Assess this cell for malaria.
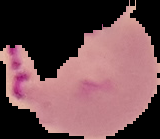

Parasitized.

Summary:
  - Preparation: thin blood film
  - Image type: cell region segmented out of the field of view; surrounding area masked to black
  - Image size: 160×139 pixels